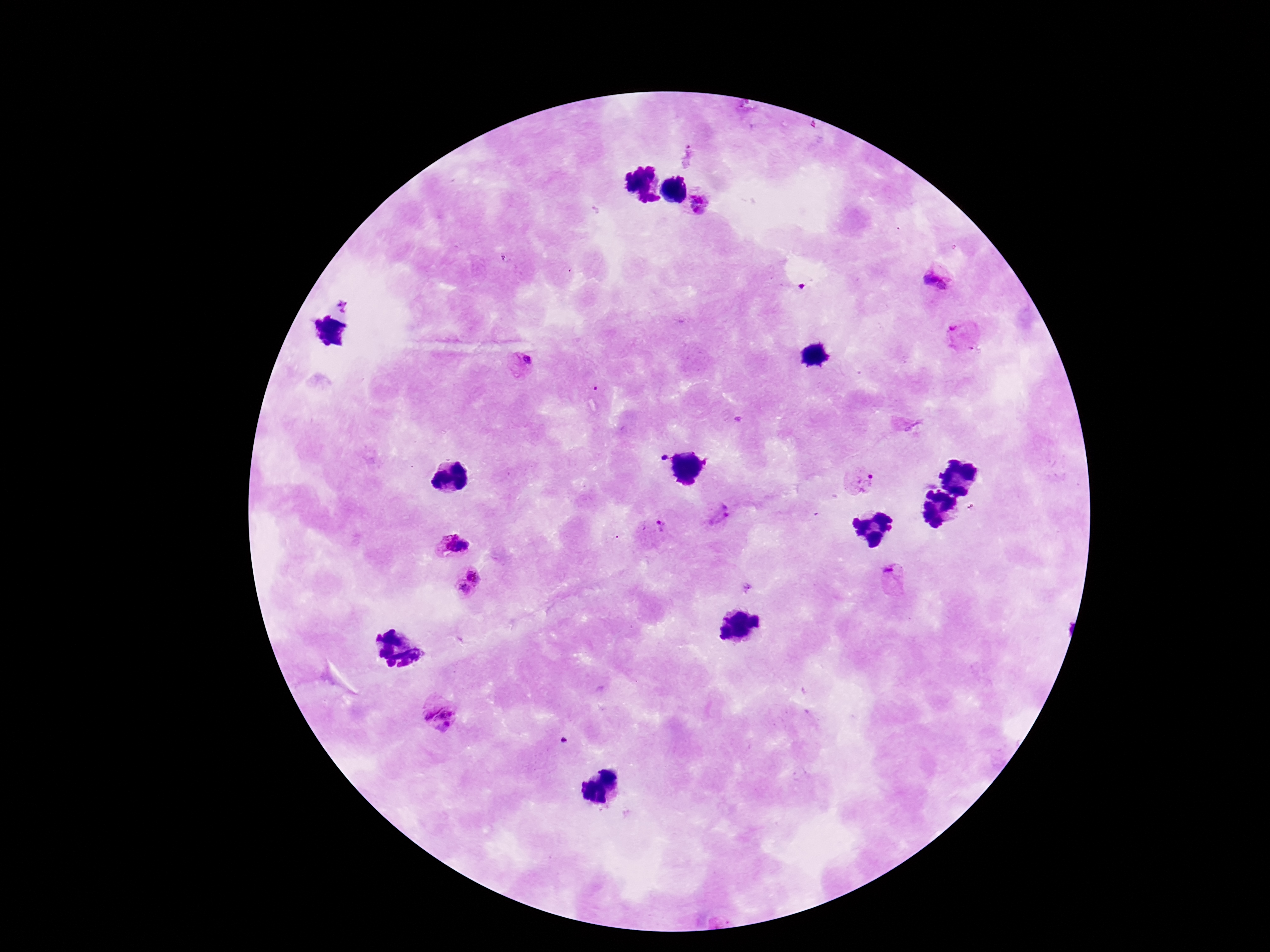 Approximate centers as {x, y} in pixels. Plasmodium parasite locations: {702, 203}, {937, 283}, {343, 305}, {960, 334}, {522, 363}, {866, 481}, {721, 512}, {661, 527}, {454, 545}, {475, 573}, {895, 576}, {745, 586}, {461, 592}, {439, 714}. 100x magnification. Thick peripheral-blood smear. Smartphone photograph taken through the microscope eyepiece. Patient malaria status: infected. Giemsa-stained preparation. Image is 1270×952 pixels. One field from this slide.